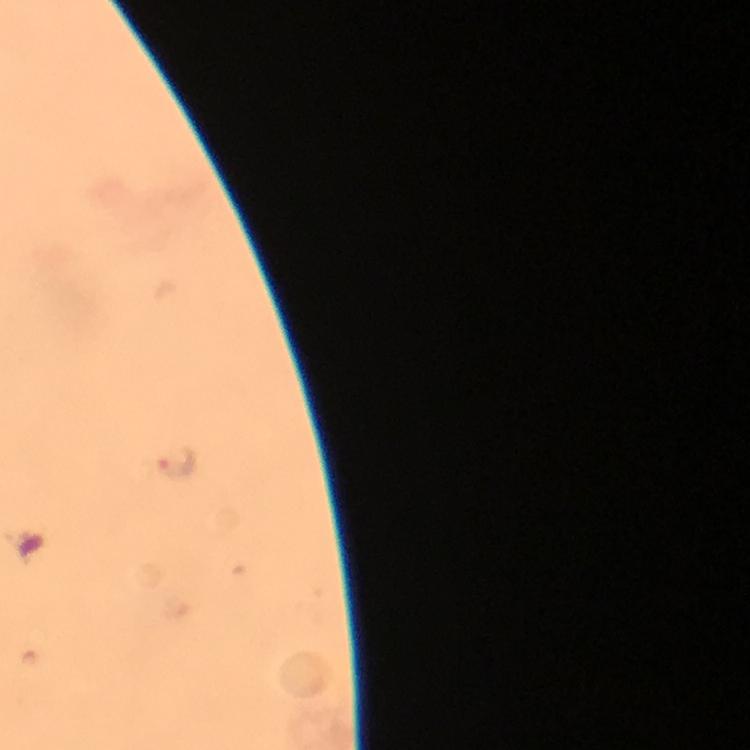 Approximate centers as {x, y} in pixels. Malaria parasite locations: {177, 466}. Image is 750×750 pixels. At 100x magnification. Thick blood film. From a malaria diagnostic workup. Smartphone photograph taken through a microscope. A crop from one field of view. Immersion oil was used. Giemsa-stained preparation.